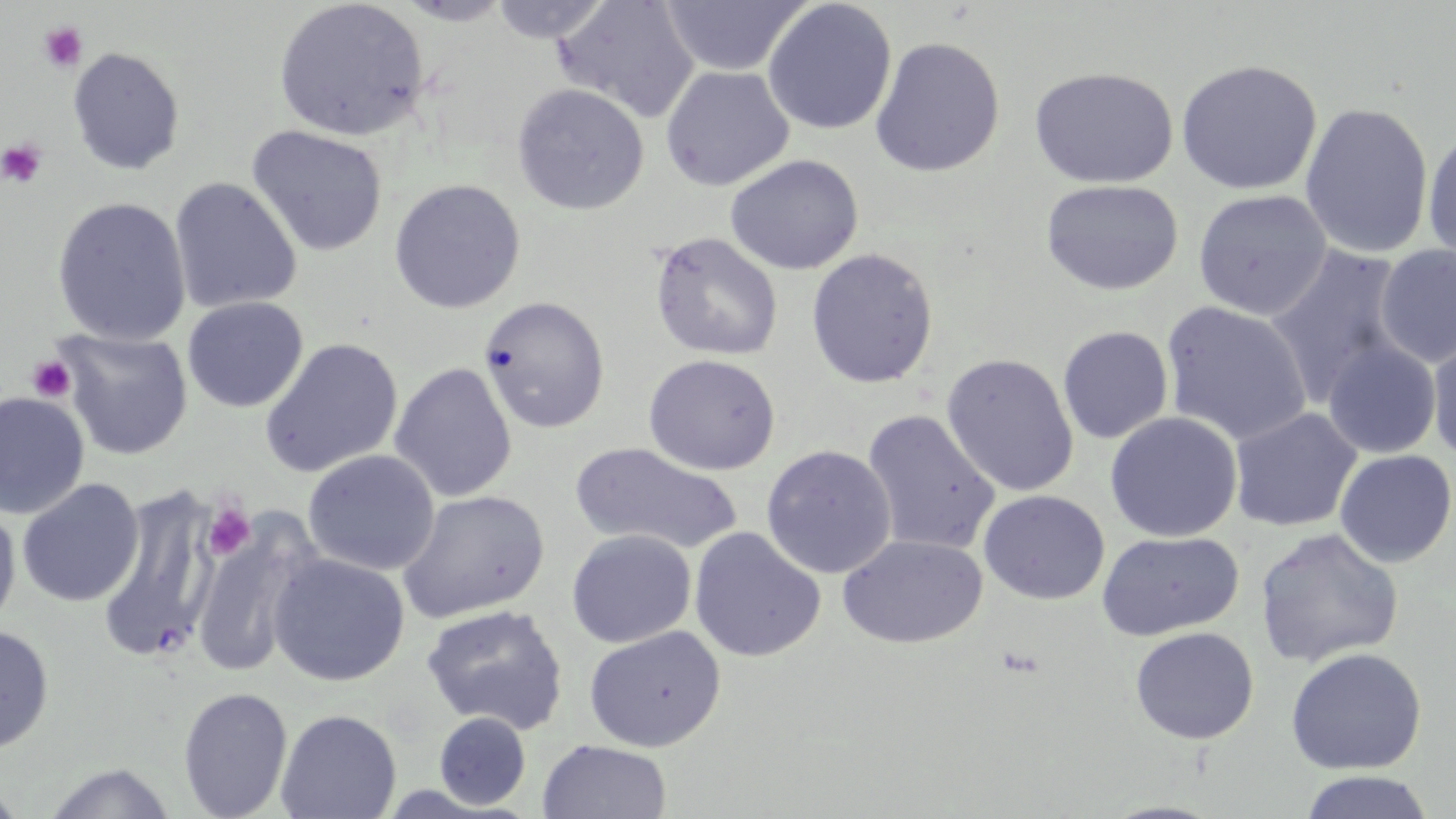

Approximate bounding boxes as [x1, y1, x2, y2] in pixels. Uninfected red blood cell locations: [394, 0, 516, 26], [488, 0, 614, 43], [659, 0, 811, 77], [762, 0, 897, 135], [272, 1, 429, 142], [552, 1, 698, 123], [869, 36, 1006, 178], [67, 46, 185, 175], [1175, 59, 1323, 195], [660, 65, 795, 191], [1029, 66, 1179, 189], [511, 83, 649, 216], [1299, 101, 1434, 259], [246, 125, 388, 258], [1422, 129, 1456, 267], [725, 154, 863, 275], [169, 177, 303, 314], [388, 178, 526, 314], [1040, 178, 1184, 296], [1192, 189, 1332, 319], [51, 196, 192, 346], [649, 231, 783, 362], [1374, 244, 1456, 367], [1264, 246, 1410, 406], [805, 248, 939, 389], [182, 296, 308, 413], [479, 296, 610, 433], [1161, 301, 1313, 447], [1057, 326, 1174, 444], [54, 328, 193, 460], [1426, 329, 1456, 466], [260, 338, 403, 478], [1322, 339, 1441, 459], [643, 353, 781, 475], [941, 353, 1079, 497], [389, 362, 517, 503], [0, 391, 90, 519], [1228, 407, 1362, 532], [862, 409, 1000, 555], [1105, 411, 1242, 542], [569, 442, 742, 555], [761, 445, 896, 578], [303, 449, 439, 575], [1334, 450, 1455, 568], [16, 478, 144, 607], [396, 489, 551, 625], [95, 490, 218, 661], [978, 490, 1110, 605], [0, 499, 21, 635], [190, 517, 318, 681], [689, 527, 826, 662], [1255, 527, 1404, 668], [566, 529, 697, 647], [1097, 531, 1244, 642], [837, 534, 987, 649], [268, 552, 409, 687], [421, 604, 569, 735], [0, 624, 54, 753], [584, 626, 726, 751], [1130, 626, 1259, 745], [1285, 648, 1427, 774], [177, 686, 293, 819], [276, 708, 402, 819], [433, 712, 531, 810], [537, 739, 671, 819], [38, 762, 179, 819], [1299, 770, 1434, 819], [0, 780, 28, 819]. Platelet locations: [38, 21, 89, 73], [1, 137, 49, 189], [27, 355, 76, 403], [203, 504, 255, 559]. Slide-level diagnosis: negative for blood parasites. Thin blood smear. Light microscopy. Captured at 1000x magnification. May-Grünwald-Giemsa stain. Image is 1456×819 pixels. Single field of view.